Locate every Plasmodium parasite and every leukocyte.
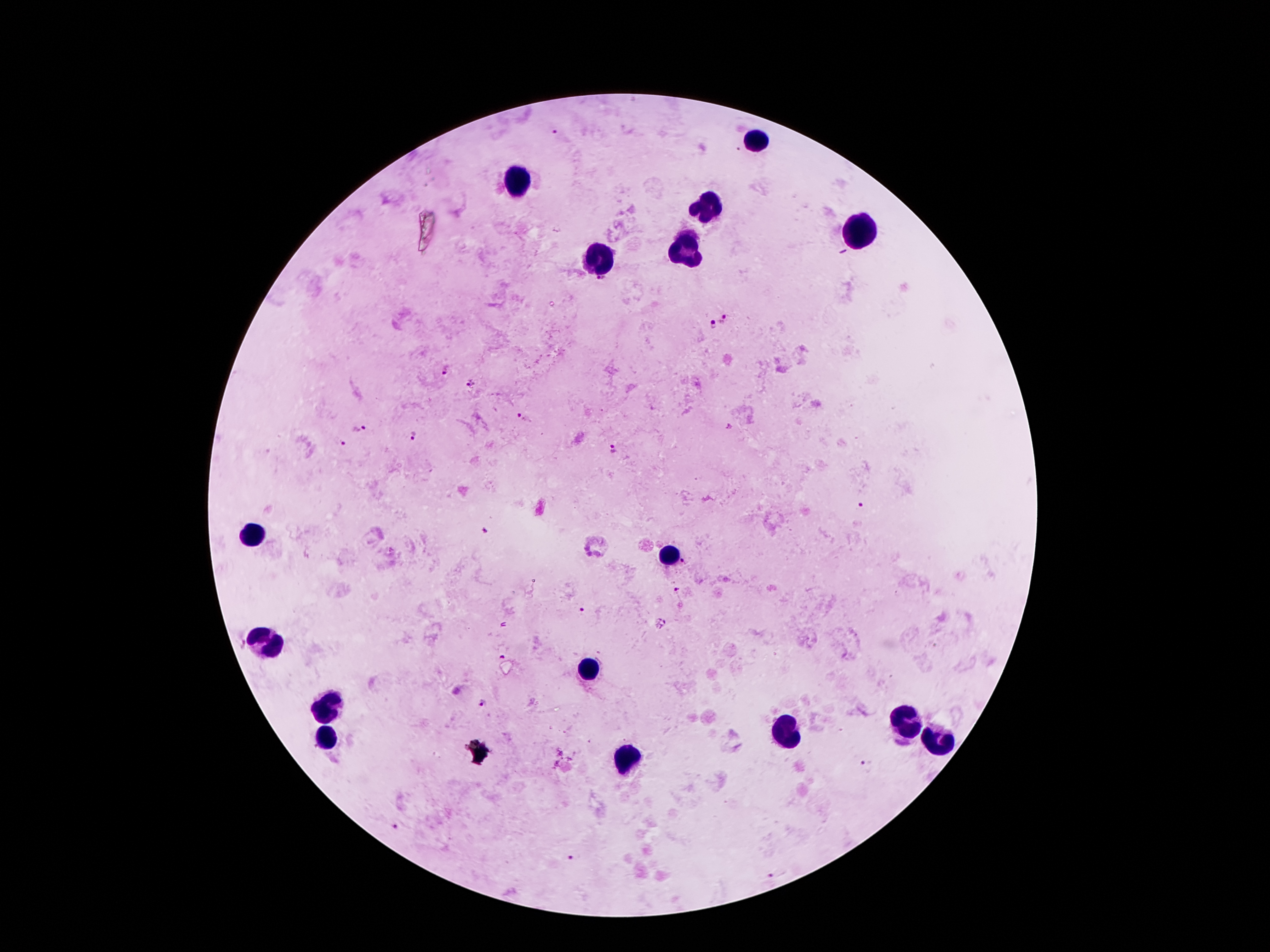
Approximate centers as [x, y] in pixels.
Plasmodium parasites: [554, 133], [723, 318], [711, 324], [442, 371], [470, 383], [520, 416], [358, 430], [412, 434], [343, 444], [614, 449], [861, 505], [684, 563], [676, 589], [584, 611], [501, 657], [482, 703], [868, 767], [394, 825], [570, 856], [776, 875].
Leukocytes: [756, 140], [519, 180], [711, 211], [862, 235], [687, 248], [599, 257], [251, 529], [669, 556], [267, 640], [588, 671], [331, 704], [906, 721], [782, 730], [324, 737], [937, 744], [630, 757].

capture: smartphone through the microscope eyepiece
image_size: 1270×952 pixels
magnification: 100x
preparation: thick blood smear
stain: Giemsa
field_of_view: single
patient_malaria_status: positive for Plasmodium falciparum